Name the cell type shown.
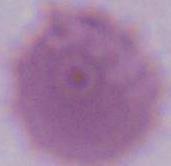
An erythrocyte.

modality = photomicrograph
magnification = 1000x